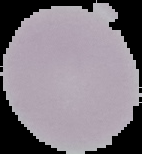
Summary:
  - Image type: segmented cell region on a black background
  - Result: negative for malaria parasites
  - Image size: 142×154 pixels
  - Preparation: thin blood film